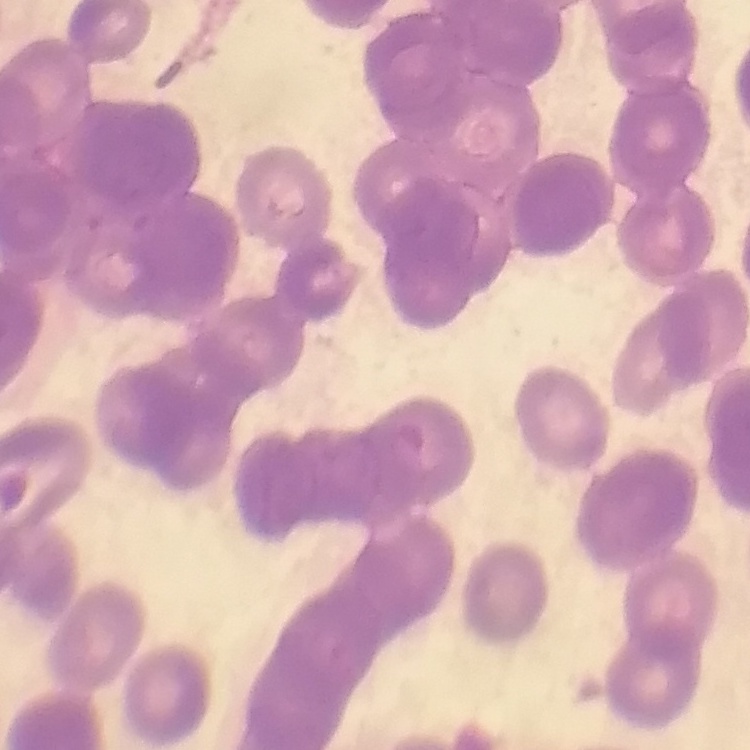
The red blood cells show rouleaux formation. Stained with either Field's or Giemsa. One tile cut from a larger photomicrograph. Thin blood smear.